Describe the morphology of the red blood cells.
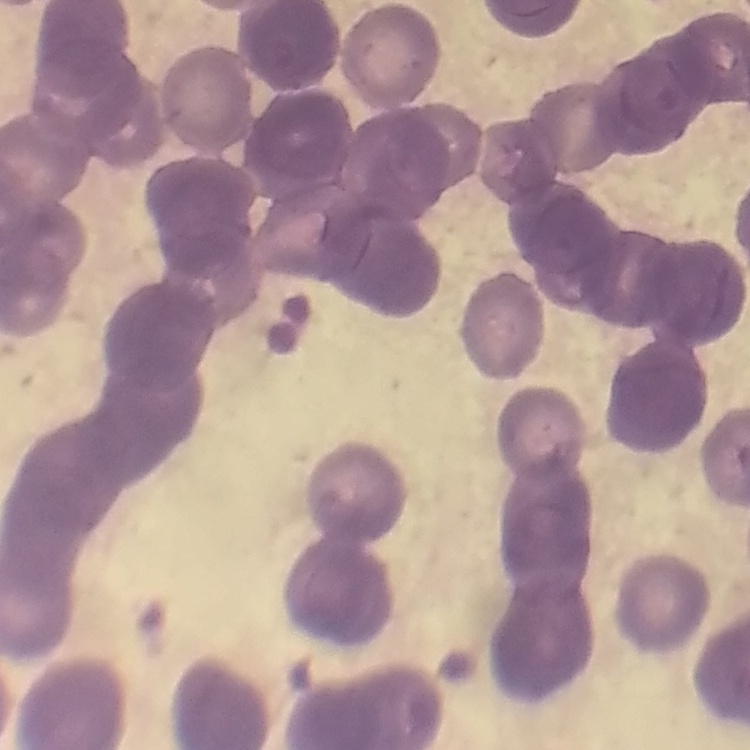
They show rouleaux formation.

preparation = thin peripheral smear
stain = Field's or Giemsa
image type = one tile cut from a larger photomicrograph